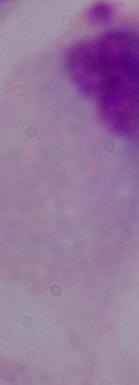 A trichomonad is shown. Micrograph. 1000x magnification.